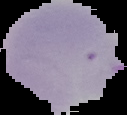
Image is 127×115 pixels. Cell region segmented out of the field of view; the surrounding area is masked to black. From a thin blood smear. Result: malaria parasites detected.